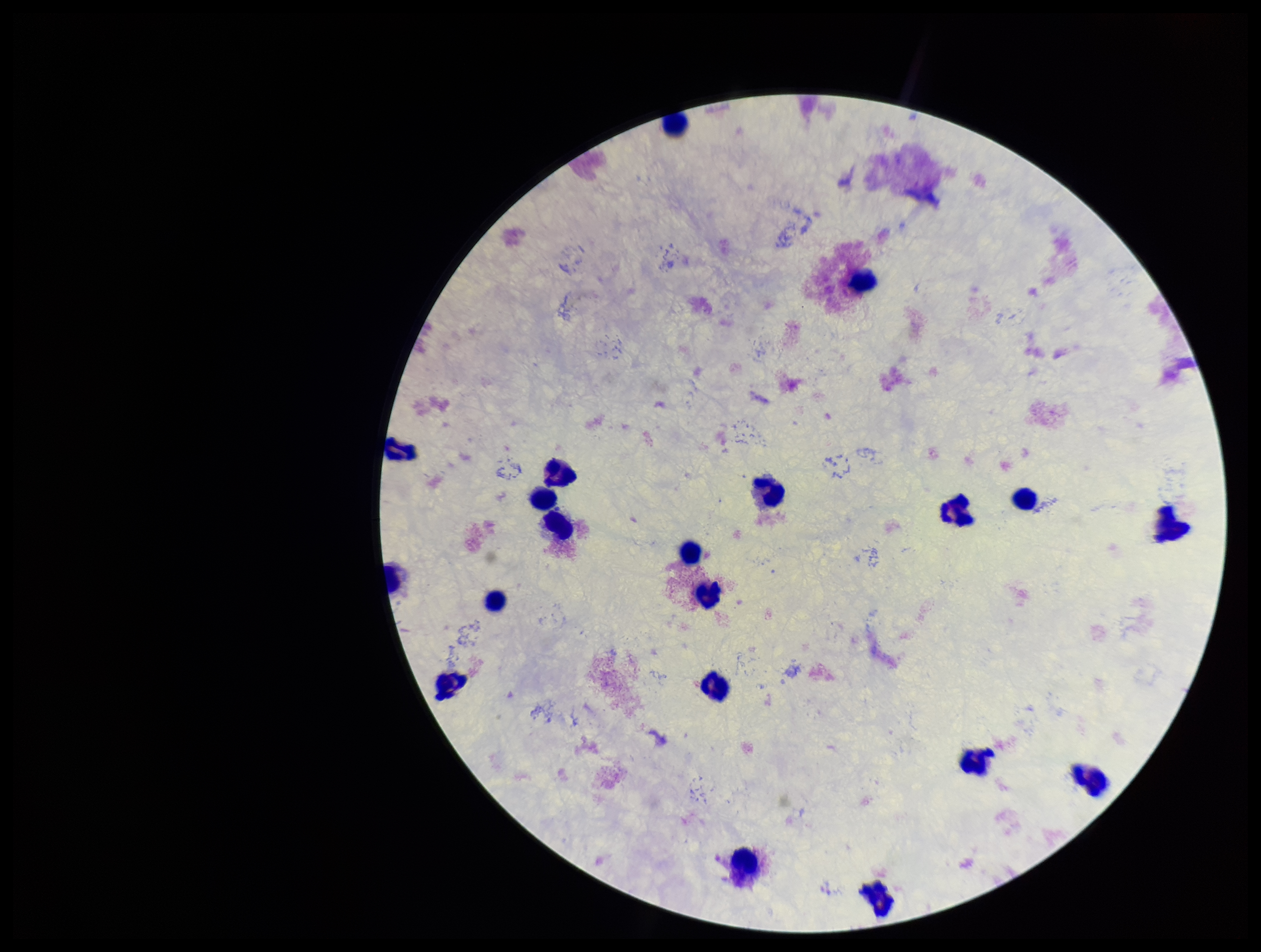

Summary:
  - Parasite count: 0
  - Plasmodium parasites: none detected
  - Preparation: thick blood smear
  - Capture: smartphone photograph through the microscope eyepiece
  - Stain: Giemsa
  - Patient malaria status: negative
  - Image size: 1261×952 pixels
  - Leukocyte count: 20
  - Field of view: single